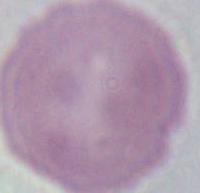

An erythrocyte is shown. Micrograph. 1000x magnification.